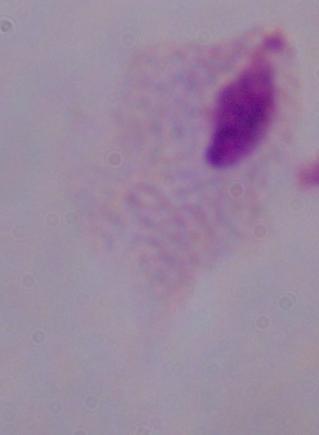 A trichomonad is seen. Photomicrograph. Captured at 1000x magnification.